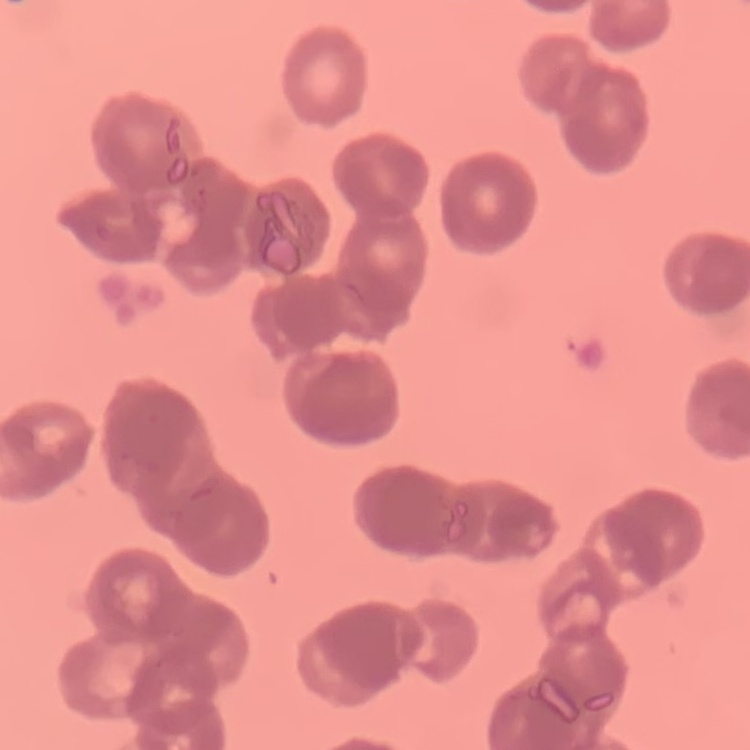
The erythrocytes exhibit rouleaux formation. One tile cut from a larger photomicrograph. Thin peripheral smear. Field's or Giemsa stain.